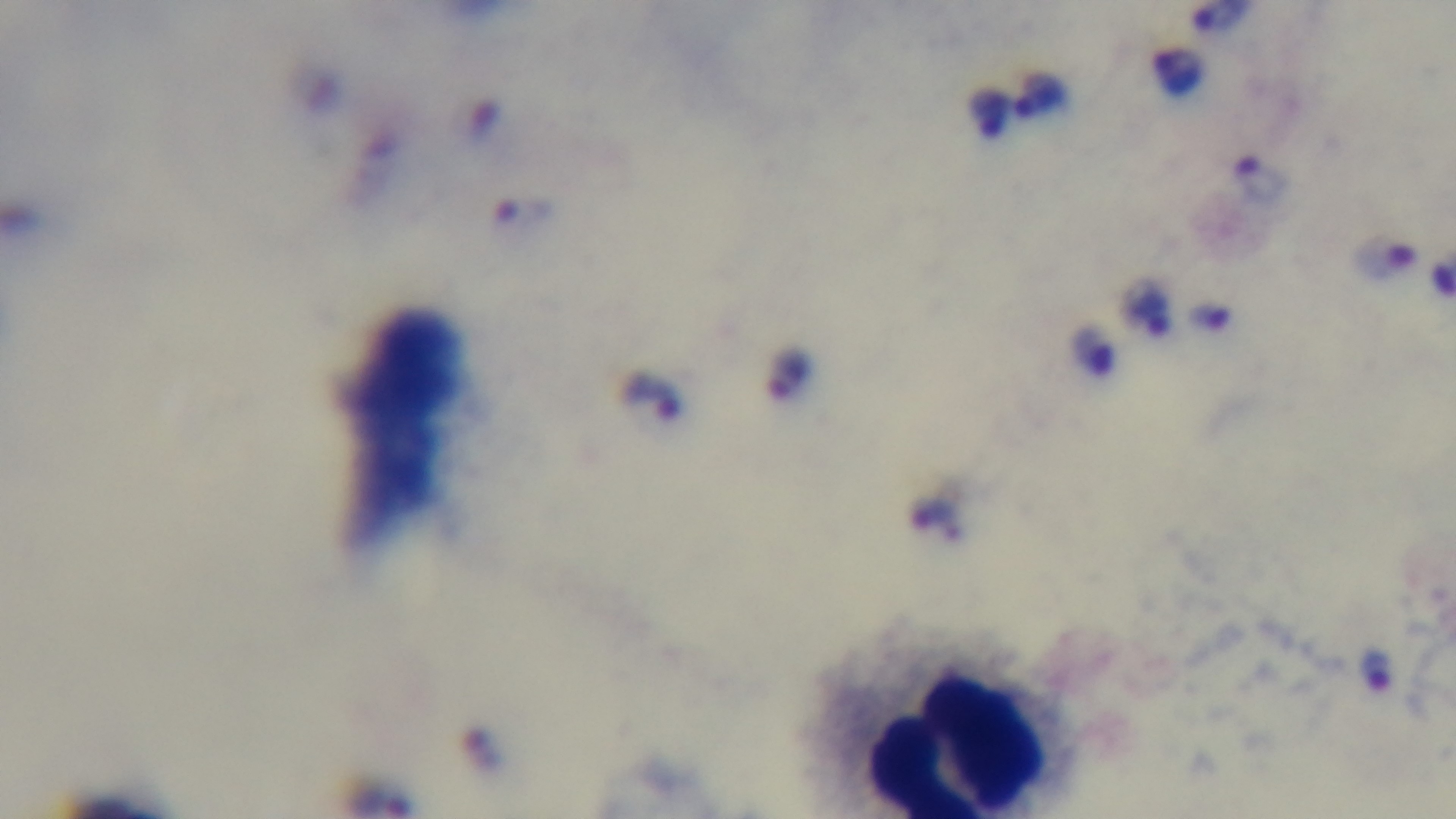
Summary:
  - Modality: light microscopy
  - Capture: mounted 4K digital camera
  - Malaria status: infected
  - Stain: Giemsa
  - Preparation: thick blood film
  - Objective: 100x oil immersion
  - Field of view: one from the slide